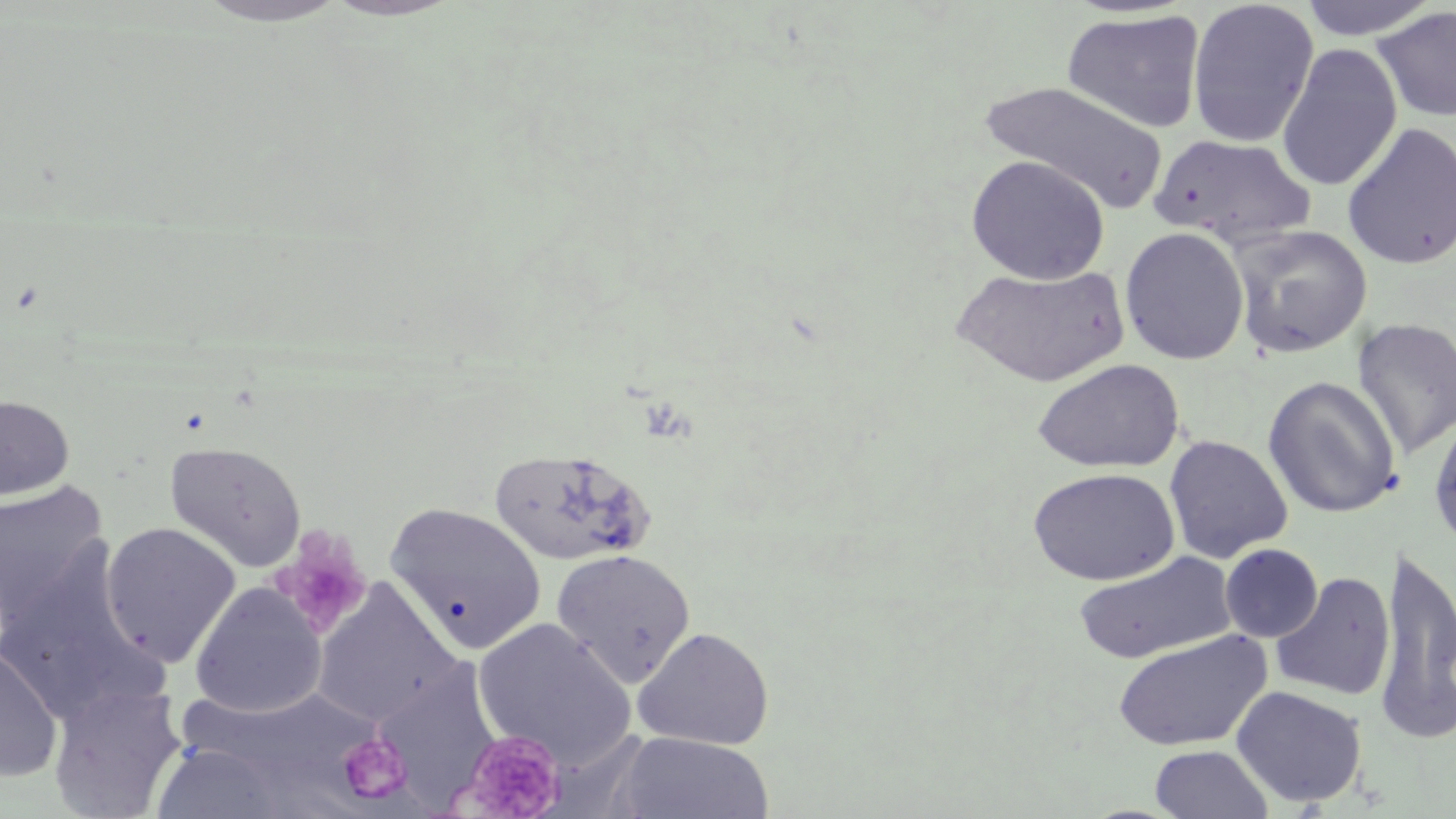
slide_level_diagnosis: no evidence of blood parasites
uninfected_red_blood_cell_locations_subset: 'approximate bounding boxes as named x1/y1/x2/y2 corners in pixels: (x1=193, y1=0, x2=351, y2=27), (x1=1296, y1=0, x2=1443, y2=41), (x1=322, y1=1, x2=460, y2=22), (x1=1186, y1=1, x2=1320, y2=148), (x1=1372, y1=7, x2=1456, y2=124), (x1=1062, y1=9, x2=1206, y2=133), (x1=1276, y1=43, x2=1403, y2=192), (x1=978, y1=79, x2=1167, y2=213), (x1=1342, y1=122, x2=1456, y2=270), (x1=1149, y1=134, x2=1316, y2=247), (x1=966, y1=154, x2=1110, y2=284), (x1=1229, y1=225, x2=1372, y2=359), (x1=1119, y1=227, x2=1250, y2=365), (x1=952, y1=263, x2=1130, y2=388), (x1=1352, y1=318, x2=1456, y2=459), (x1=1031, y1=358, x2=1185, y2=473), (x1=1263, y1=376, x2=1401, y2=518), (x1=0, y1=395, x2=75, y2=500), (x1=1427, y1=409, x2=1456, y2=550), (x1=1164, y1=435, x2=1293, y2=564), (x1=165, y1=440, x2=307, y2=572), (x1=486, y1=445, x2=654, y2=567), (x1=1027, y1=467, x2=1181, y2=586), (x1=0, y1=480, x2=110, y2=626), (x1=385, y1=502, x2=547, y2=653), (x1=100, y1=522, x2=241, y2=666), (x1=1220, y1=544, x2=1323, y2=643), (x1=1373, y1=548, x2=1456, y2=745), (x1=551, y1=549, x2=696, y2=687), (x1=1071, y1=551, x2=1236, y2=665), (x1=0, y1=553, x2=164, y2=725), (x1=1270, y1=571, x2=1396, y2=701), (x1=312, y1=581, x2=461, y2=727), (x1=189, y1=583, x2=326, y2=718), (x1=633, y1=626, x2=775, y2=750), (x1=1112, y1=629, x2=1271, y2=752), (x1=0, y1=644, x2=63, y2=782), (x1=48, y1=684, x2=187, y2=818), (x1=1231, y1=685, x2=1368, y2=807), (x1=178, y1=686, x2=377, y2=790), (x1=613, y1=733, x2=775, y2=818), (x1=150, y1=742, x2=291, y2=819), (x1=1150, y1=745, x2=1273, y2=819)'
magnification: 1000x
stain: May-Grünwald-Giemsa
platelet_locations_subset: 'approximate bounding boxes as named x1/y1/x2/y2 corners in pixels: (x1=273, y1=529, x2=372, y2=635), (x1=458, y1=728, x2=568, y2=819), (x1=337, y1=732, x2=413, y2=805)'
field_of_view: single
image_size: 1456×819 pixels
modality: light microscopy
preparation: thin blood film